Classify this cell by malaria status.
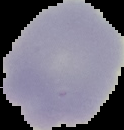

It is uninfected.

image type = segmented cell region with the area outside set to black
image size = 124×130 pixels
preparation = thin blood film